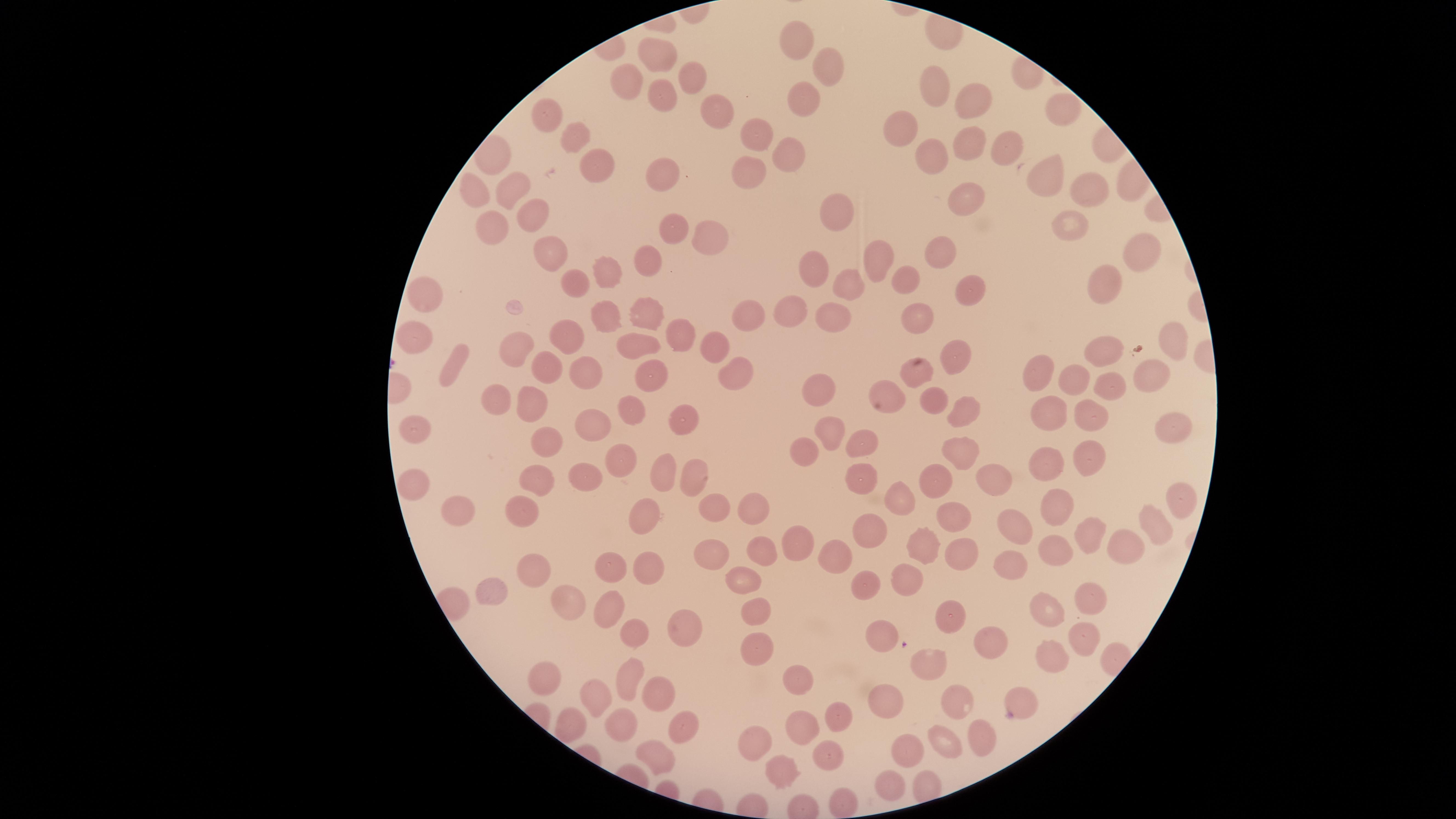
presence: no malaria parasites detected
field_of_view: single
stain: Giemsa
preparation: thin blood film
uninfected_RBCs: 'approximate marker points as [x, y] in pixels: [792, 39], [658, 52], [826, 65], [693, 75], [615, 80], [935, 91], [655, 94], [970, 99], [809, 101], [1059, 109], [709, 111], [547, 115], [901, 129], [751, 131], [570, 135], [969, 143], [1003, 144], [785, 153], [501, 156], [597, 156], [930, 156], [664, 168], [749, 173], [1052, 175], [509, 185], [476, 189], [1088, 190], [963, 192], [835, 212], [489, 218], [539, 218], [1068, 219], [668, 227], [711, 236], [551, 248], [938, 248], [1136, 255], [655, 256], [874, 256], [807, 268], [605, 270], [568, 277], [912, 277], [851, 282], [970, 283], [1107, 286], [427, 293], [646, 308], [601, 312], [793, 312], [748, 314], [918, 318], [826, 320], [560, 333], [680, 335], [1178, 342], [719, 344], [424, 346], [519, 346], [639, 347], [954, 347], [1105, 349], [456, 362], [732, 366], [545, 368], [1032, 369], [650, 373], [914, 375], [587, 376], [1153, 377], [1078, 382], [822, 389], [1116, 389], [888, 390], [498, 393], [935, 402], [539, 405], [956, 407], [1095, 409], [628, 410], [1053, 411], [593, 417], [676, 417], [1172, 424], [832, 427], [416, 431], [547, 442], [862, 442], [803, 449], [961, 457], [617, 458], [1094, 458], [1038, 467], [669, 472], [589, 473], [694, 475], [862, 477], [990, 477], [417, 481], [537, 481], [936, 483], [1175, 497], [903, 498], [1051, 501], [715, 506], [754, 508], [456, 509], [952, 510], [1014, 517], [527, 522], [651, 522], [1157, 524], [871, 530], [1088, 530], [1123, 543], [925, 546], [804, 548], [711, 549], [759, 549], [1051, 551], [967, 552], [839, 556], [1013, 559], [650, 564], [536, 569], [601, 573], [742, 578], [906, 578], [863, 581], [489, 588], [569, 591], [1084, 595], [754, 606], [603, 609], [1043, 610], [950, 617], [681, 625], [1080, 631], [630, 633], [880, 636], [988, 637], [754, 642], [1051, 656], [932, 666], [626, 676], [549, 680], [802, 685], [595, 691], [655, 694], [952, 698], [884, 700], [1020, 701], [838, 716], [808, 726], [686, 727], [627, 728], [976, 735], [756, 740], [942, 741], [828, 748], [904, 753], [668, 757], [780, 769], [890, 785], [845, 804]'
visible_region: circular
capture: smartphone photograph through the microscope eyepiece
image_size: 1456×819 pixels